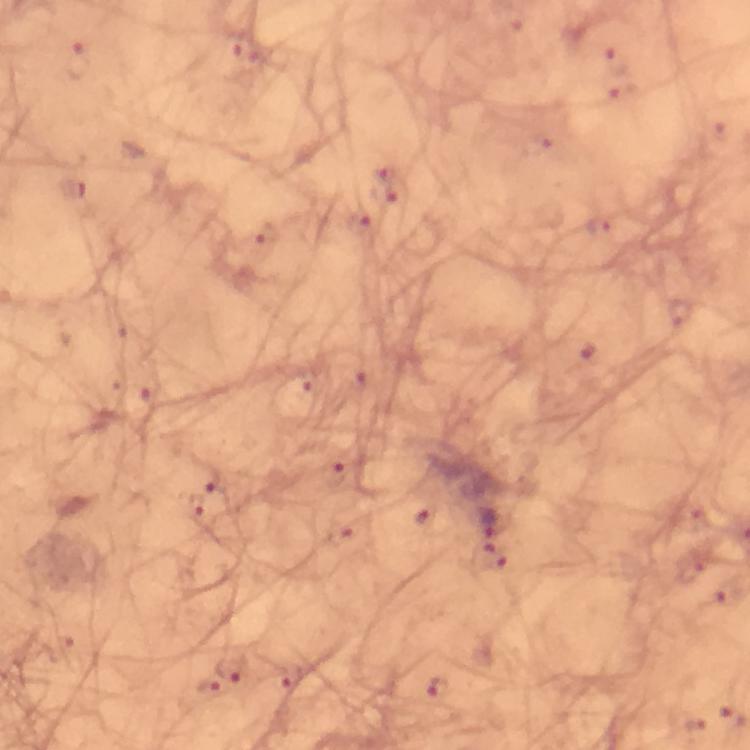 Approximate centers as [x, y] in pixels. Malaria parasite locations: [77, 59], [383, 172], [384, 192], [265, 237], [333, 476], [194, 504], [486, 520], [339, 531], [494, 557], [230, 666], [434, 688]. Image is 750×750 pixels. Photographed with a smartphone mounted on the microscope. Giemsa-stained preparation. 100x magnification. Thick blood smear. Cropped region of a single field of view. From a diagnostic examination for malaria. Immersion oil applied.